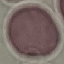 Malaria status: uninfected. Acquired by smartphone through the microscope eyepiece. Giemsa stain. Automatically extracted cell patch, resized to 64 × 64 pixels. Thin smear of blood.